Classify this cell by malaria status.
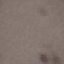
Uninfected.

Summary:
  - Preparation: thin blood film
  - Capture: smartphone through the microscope eyepiece
  - Stain: Giemsa
  - Image type: cell patch, automatically extracted from a larger field of view and resized to 64 × 64 pixels